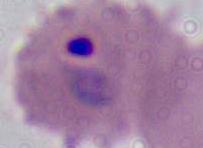 A Plasmodium parasite is shown. 400x or 1000x magnification. Micrograph.